Identify the parasite.
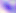
This is Toxoplasma gondii.

Summary:
  - Magnification: 400x
  - Modality: photomicrograph